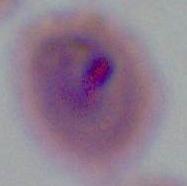
Photomicrograph. Captured at either 400x or 1000x magnification. A Plasmodium parasite is seen.